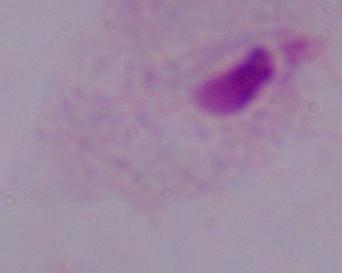
{
  "identification": "trichomonad",
  "modality": "micrograph",
  "magnification": "1000x"
}